Outline each blood parasite and name the species.
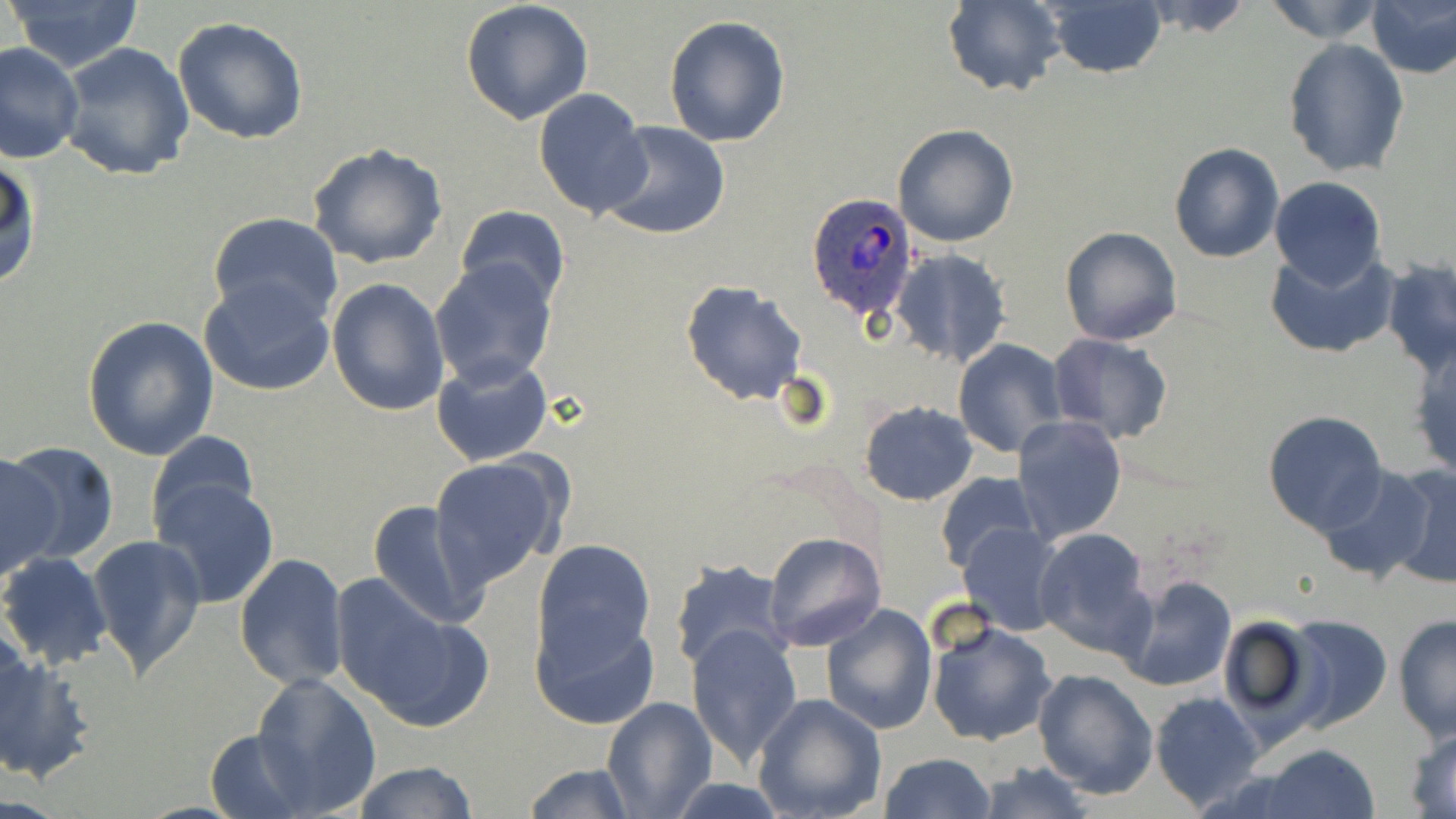

Approximate bounding boxes as named x1/y1/x2/y2 corners in pixels.
Plasmodium ovale-infected red blood cells: (x1=808, y1=194, x2=917, y2=319).
No Plasmodium falciparum, Plasmodium malariae, Plasmodium vivax, Babesia divergens, or Trypanosoma brucei observed.

Summary:
  - Uninfected red blood cell locations: (x1=4, y1=0, x2=147, y2=73), (x1=461, y1=0, x2=595, y2=126), (x1=1139, y1=0, x2=1256, y2=37), (x1=1258, y1=0, x2=1390, y2=45), (x1=940, y1=1, x2=1065, y2=95), (x1=1041, y1=1, x2=1167, y2=79), (x1=1368, y1=2, x2=1456, y2=78), (x1=664, y1=15, x2=791, y2=146), (x1=172, y1=16, x2=310, y2=145), (x1=1282, y1=38, x2=1409, y2=177), (x1=1, y1=41, x2=85, y2=167), (x1=56, y1=42, x2=196, y2=182), (x1=533, y1=88, x2=653, y2=217), (x1=597, y1=122, x2=731, y2=241), (x1=892, y1=123, x2=1019, y2=248), (x1=307, y1=140, x2=448, y2=269), (x1=1168, y1=142, x2=1284, y2=263), (x1=0, y1=155, x2=42, y2=293), (x1=1270, y1=177, x2=1386, y2=288), (x1=456, y1=205, x2=570, y2=308), (x1=208, y1=211, x2=343, y2=326), (x1=1059, y1=226, x2=1183, y2=346), (x1=1267, y1=247, x2=1398, y2=360), (x1=891, y1=249, x2=1013, y2=370), (x1=1382, y1=256, x2=1456, y2=376), (x1=430, y1=258, x2=558, y2=388), (x1=199, y1=275, x2=335, y2=396), (x1=327, y1=277, x2=449, y2=416), (x1=682, y1=280, x2=807, y2=405), (x1=81, y1=315, x2=220, y2=460), (x1=1046, y1=333, x2=1174, y2=445), (x1=953, y1=338, x2=1068, y2=458), (x1=1406, y1=338, x2=1456, y2=482), (x1=432, y1=355, x2=554, y2=466), (x1=859, y1=400, x2=977, y2=505), (x1=1262, y1=411, x2=1387, y2=535), (x1=1012, y1=416, x2=1127, y2=544), (x1=146, y1=430, x2=260, y2=537), (x1=1, y1=442, x2=118, y2=567), (x1=0, y1=451, x2=58, y2=583), (x1=430, y1=455, x2=569, y2=589), (x1=1382, y1=462, x2=1456, y2=591), (x1=1315, y1=463, x2=1437, y2=584), (x1=934, y1=470, x2=1044, y2=574), (x1=149, y1=477, x2=278, y2=609), (x1=368, y1=500, x2=491, y2=630), (x1=958, y1=521, x2=1066, y2=635), (x1=1032, y1=526, x2=1157, y2=657), (x1=762, y1=531, x2=887, y2=652), (x1=86, y1=534, x2=207, y2=680), (x1=530, y1=539, x2=657, y2=673), (x1=0, y1=552, x2=112, y2=670), (x1=234, y1=553, x2=348, y2=691), (x1=669, y1=557, x2=790, y2=673), (x1=1115, y1=571, x2=1237, y2=692), (x1=331, y1=577, x2=491, y2=732), (x1=822, y1=603, x2=937, y2=735), (x1=529, y1=606, x2=659, y2=731), (x1=1278, y1=614, x2=1393, y2=734), (x1=1392, y1=614, x2=1455, y2=740), (x1=1213, y1=615, x2=1323, y2=735), (x1=925, y1=617, x2=1058, y2=748), (x1=686, y1=623, x2=804, y2=765), (x1=0, y1=645, x2=93, y2=784), (x1=1032, y1=668, x2=1159, y2=798), (x1=251, y1=672, x2=382, y2=814), (x1=1150, y1=691, x2=1266, y2=813), (x1=753, y1=693, x2=888, y2=819), (x1=600, y1=696, x2=717, y2=818), (x1=1404, y1=726, x2=1456, y2=817), (x1=205, y1=727, x2=312, y2=816), (x1=1257, y1=744, x2=1381, y2=819), (x1=881, y1=752, x2=997, y2=819), (x1=350, y1=760, x2=478, y2=818), (x1=974, y1=760, x2=1096, y2=819), (x1=523, y1=761, x2=638, y2=818), (x1=661, y1=778, x2=795, y2=818)
  - Slide-level diagnosis: Plasmodium ovale
  - Magnification: 1000x
  - Modality: light microscopy
  - Field of view: one of a larger specimen
  - Stain: May-Grünwald-Giemsa
  - Image size: 1456×819 pixels
  - Preparation: thin blood film